State the preparation type.
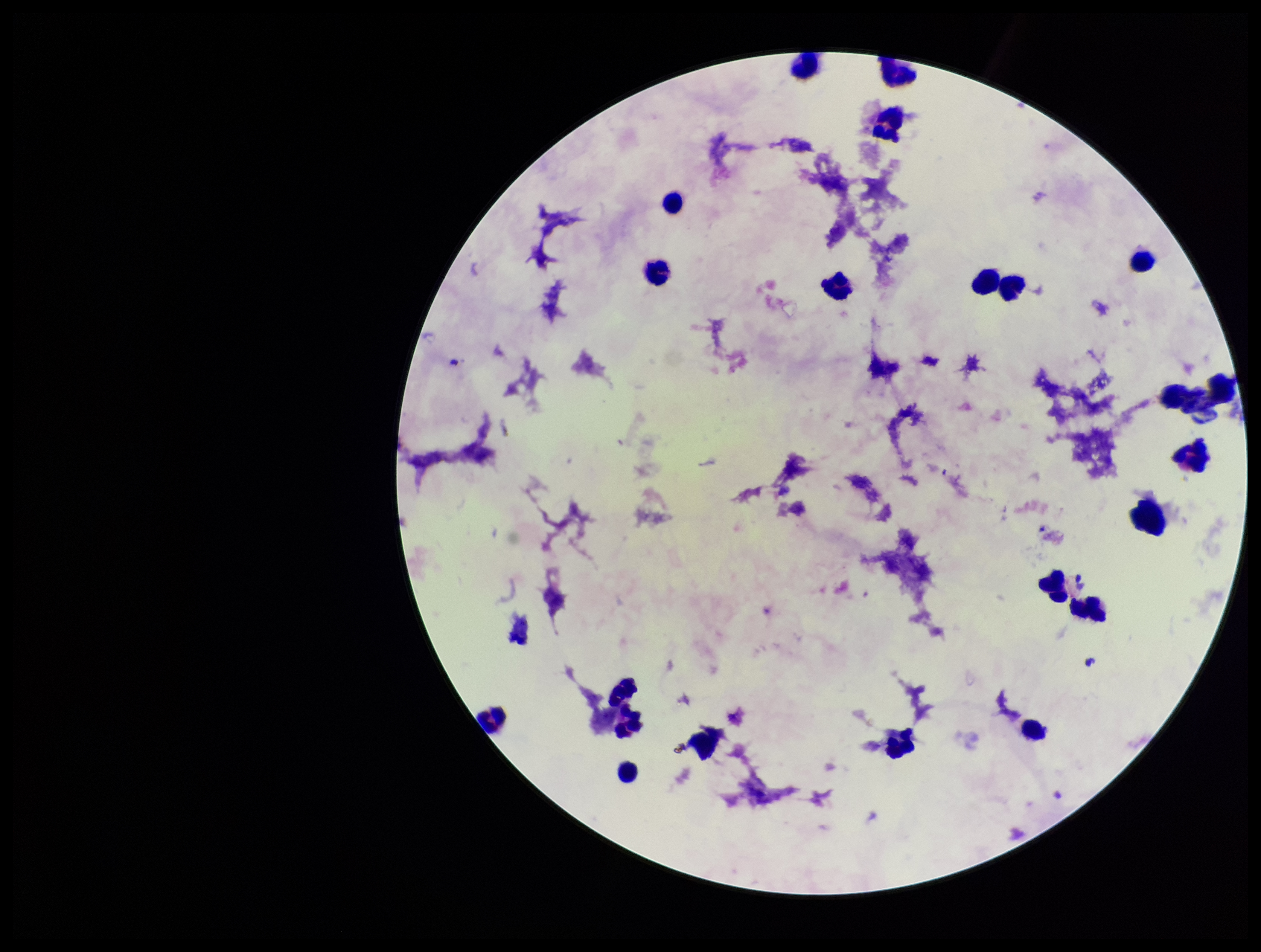

Thick.

{
  "plasmodium_parasites": "none detected",
  "patient_malaria_status": "negative",
  "capture": "smartphone photograph through the microscope eyepiece",
  "image_size": "1261×952 pixels",
  "stain": "Giemsa",
  "leukocyte_count": 20,
  "field_of_view": "one from this slide",
  "parasite_count": 0
}